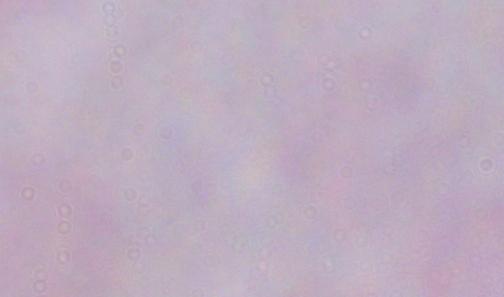 A trypanosome is seen. Micrograph. Captured at 1000x magnification.